Name the parasite shown.
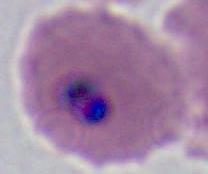
Plasmodium.

Summary:
  - Modality: photomicrograph
  - Magnification: 400x or 1000x